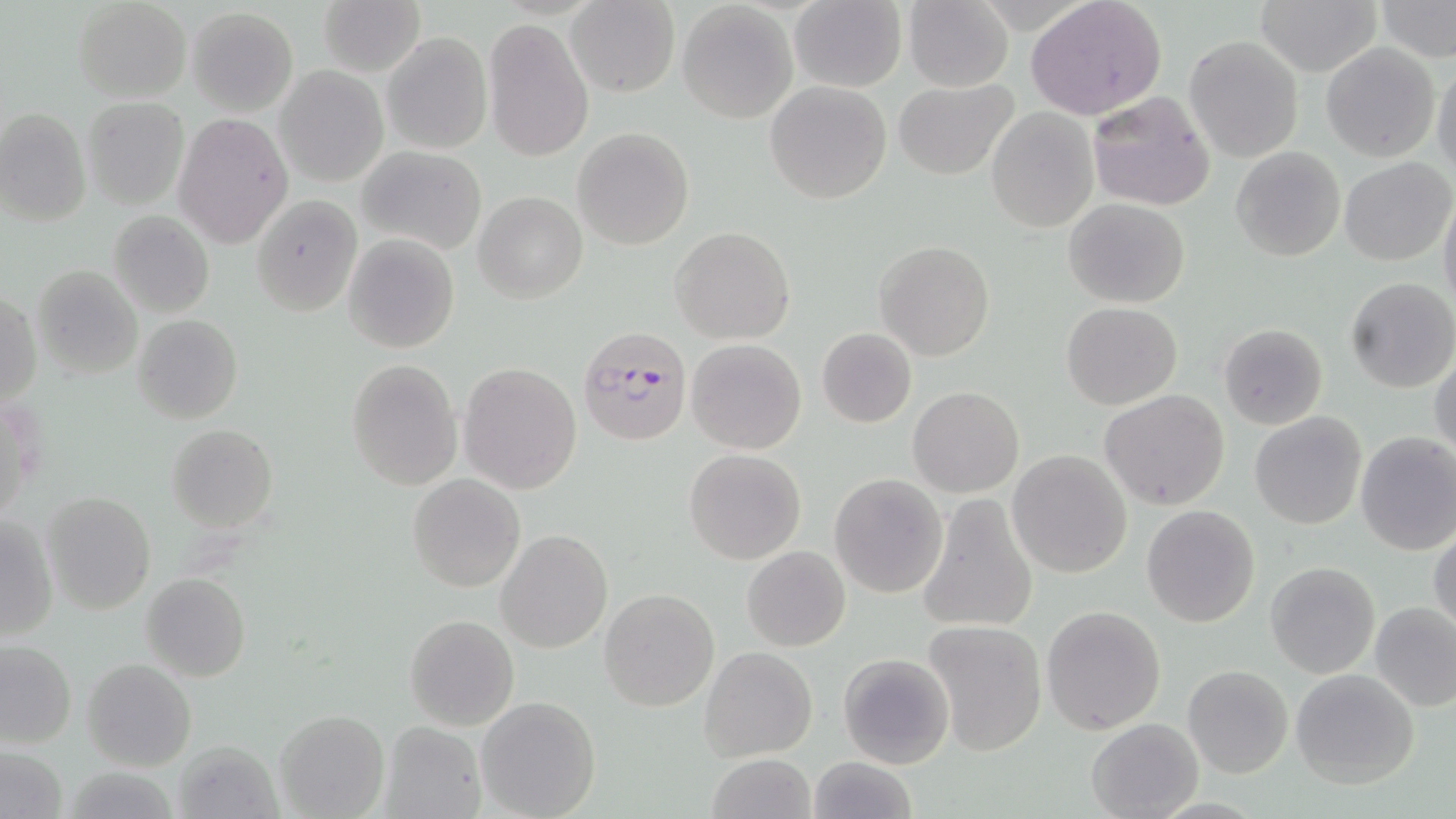
Approximate bounding boxes as (x1, y1, x2, y2) in pixels. Plasmodium falciparum-infected red blood cell locations: (576, 326, 690, 448). Uninfected red blood cell locations: (72, 0, 191, 101), (318, 0, 425, 76), (789, 0, 907, 92), (903, 0, 1015, 91), (1026, 0, 1167, 120), (1256, 0, 1382, 75), (1374, 0, 1455, 61), (565, 1, 680, 96), (678, 2, 798, 122), (187, 7, 297, 114), (482, 20, 595, 162), (381, 31, 492, 155), (1183, 36, 1304, 162), (1322, 43, 1440, 161), (1432, 56, 1456, 179), (275, 66, 388, 187), (892, 78, 1019, 180), (764, 81, 892, 204), (1086, 92, 1216, 211), (83, 98, 188, 209), (0, 108, 91, 227), (986, 109, 1097, 232), (172, 112, 293, 249), (572, 129, 693, 249), (1229, 145, 1345, 262), (357, 147, 487, 255), (1339, 159, 1454, 266), (1439, 185, 1456, 314), (475, 192, 587, 303), (252, 194, 361, 316), (1063, 198, 1190, 308), (108, 211, 214, 318), (670, 227, 794, 345), (343, 233, 460, 353), (874, 240, 995, 362), (31, 264, 143, 379), (1345, 277, 1456, 393), (2, 290, 40, 409), (1061, 302, 1183, 409), (133, 315, 243, 423), (1218, 322, 1329, 431), (817, 328, 917, 428), (686, 338, 806, 455), (1431, 352, 1456, 460), (346, 359, 463, 489), (459, 363, 582, 494), (908, 386, 1024, 498), (1100, 390, 1231, 511), (1249, 411, 1367, 530), (167, 424, 278, 532), (1355, 431, 1456, 555), (684, 449, 805, 564), (1008, 449, 1132, 578), (408, 474, 525, 592), (830, 474, 948, 598), (43, 490, 156, 615), (915, 495, 1039, 635), (1141, 504, 1260, 628), (1, 516, 59, 642), (1429, 528, 1456, 637), (497, 529, 613, 652), (742, 545, 851, 651), (1266, 561, 1379, 677), (141, 573, 250, 681), (599, 589, 718, 711), (1371, 600, 1456, 711), (1041, 604, 1166, 734), (405, 615, 519, 729), (922, 619, 1049, 757), (1, 640, 76, 749), (700, 647, 818, 761), (838, 654, 955, 768), (82, 658, 196, 771), (1182, 664, 1294, 779), (1290, 668, 1421, 788), (476, 696, 601, 819), (274, 709, 388, 819), (1086, 718, 1203, 819), (379, 721, 487, 819), (171, 739, 284, 819), (1, 747, 67, 819), (703, 754, 816, 819), (805, 757, 918, 818). Slide-level diagnosis: Plasmodium falciparum. Image is 1456×819 pixels. May-Grünwald-Giemsa stain. Light microscopy. Captured at 1000x magnification. Thin blood film. One field of a larger specimen.